Name the parasite shown.
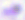
Toxoplasma gondii.

modality = micrograph
magnification = 400x